Identify the parasite.
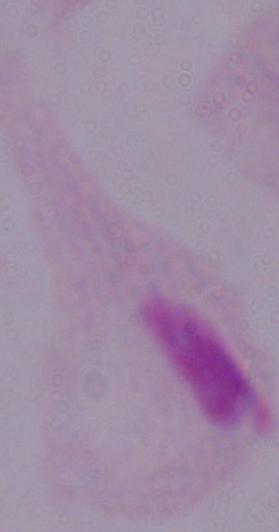
A trichomonad.

{
  "magnification": "1000x",
  "modality": "micrograph"
}